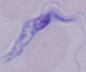

modality = micrograph
magnification = 1000x
identification = trypanosome